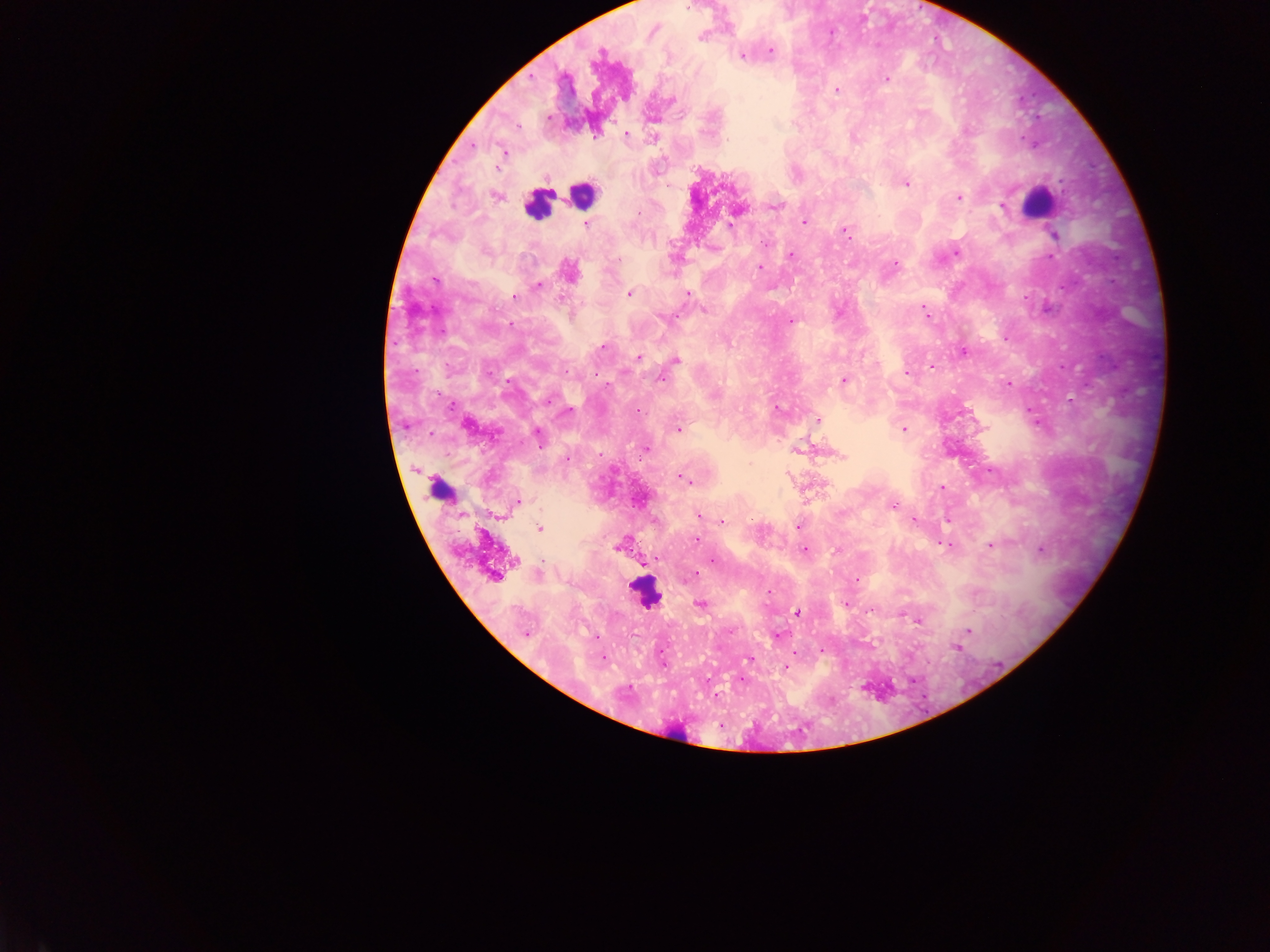
image size = 1270×952 pixels
preparation = thick blood smear
field of view = single
capture = mobile-phone photograph through a microscope
country = Ghana
leukocyte locations = approximate centers as {x, y} in pixels: {582, 194}, {1040, 202}, {536, 205}, {439, 490}, {645, 593}, {674, 734}
malaria parasite locations = approximate centers as {x, y} in pixels: {688, 6}, {831, 32}, {701, 37}, {771, 51}, {742, 56}, {887, 80}, {836, 89}, {671, 100}, {627, 134}, {595, 137}, {726, 141}, {504, 151}, {906, 183}, {497, 196}, {958, 198}, {775, 206}, {1002, 206}, {804, 222}, {586, 224}, {730, 226}, {847, 232}, {1055, 235}, {955, 253}, {791, 255}, {1053, 256}, {895, 263}, {760, 267}, {568, 271}, {435, 280}, {538, 286}, {629, 293}, {688, 294}, {515, 297}, {704, 310}, {925, 312}, {663, 318}, {791, 321}, {1005, 338}, {604, 347}, {963, 352}, {638, 357}, {676, 360}, {930, 367}, {1062, 367}, {907, 373}, {661, 378}, {843, 380}, {1009, 383}, {508, 384}, {548, 400}, {777, 408}, {637, 411}, {568, 412}, {818, 420}, {467, 425}, {678, 429}, {903, 429}, {538, 435}, {646, 448}, {840, 455}, {683, 478}, {942, 487}, {518, 501}, {893, 506}, {698, 516}, {915, 520}, {722, 521}, {798, 527}, {540, 528}, {696, 540}, {945, 545}, {991, 545}, {619, 546}, {804, 550}, {836, 550}, {1040, 550}, {713, 560}, {514, 561}, {694, 574}, {495, 576}, {857, 580}, {769, 593}, {700, 604}, {846, 604}, {871, 611}, {797, 613}, {919, 620}, {730, 630}, {968, 631}, {525, 634}, {779, 635}, {956, 648}, {822, 650}, {749, 660}, {786, 667}, {741, 681}, {716, 695}